Locate every Plasmodium parasite.
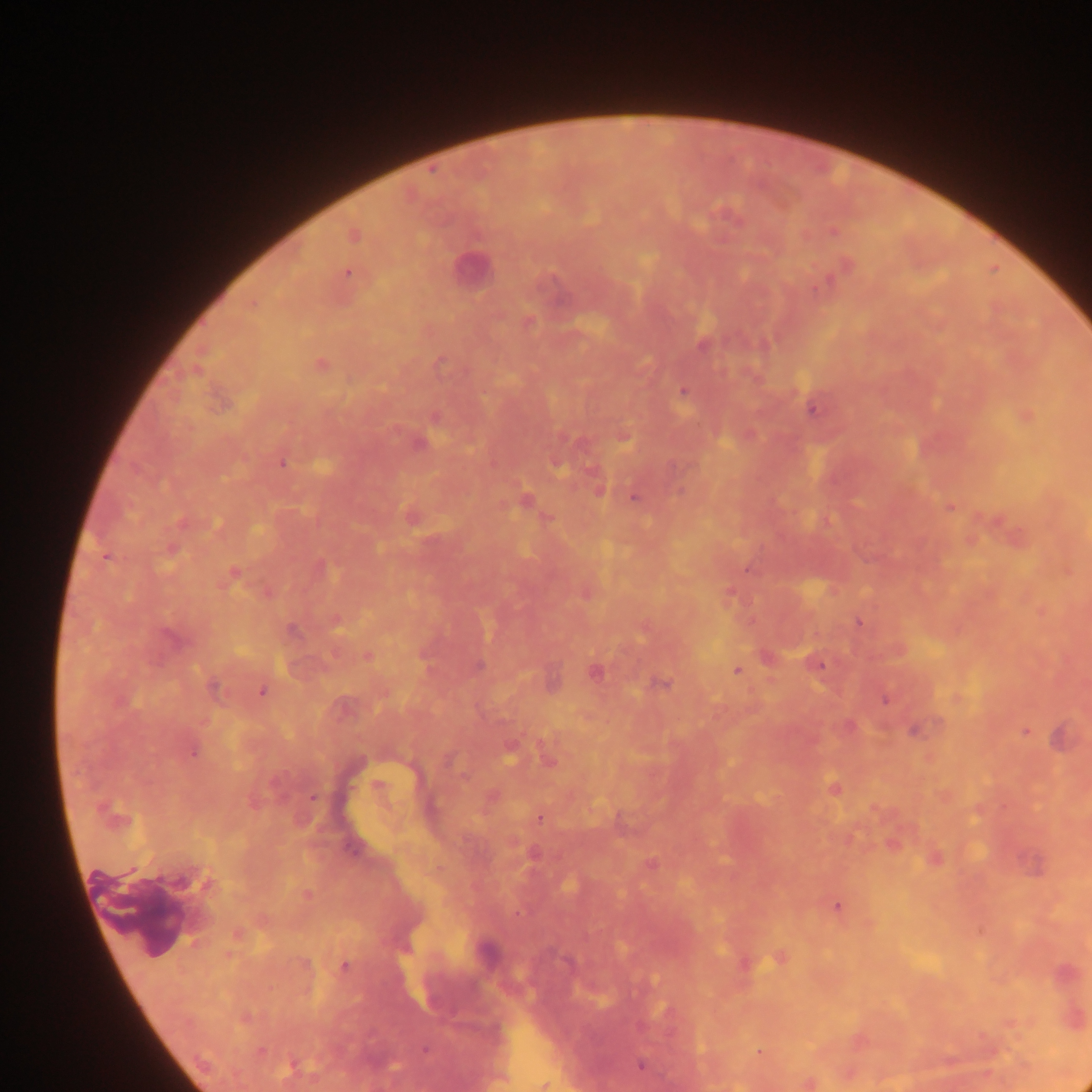

Approximate centers as [x, y] in pixels.
Plasmodium parasites: [727, 217], [834, 233], [353, 235], [847, 264], [347, 273], [527, 322], [702, 346], [320, 365], [684, 391], [812, 410], [436, 417], [623, 437], [419, 443], [282, 464], [556, 465], [599, 491], [679, 493], [634, 498], [524, 501], [950, 506], [106, 557], [233, 573], [859, 622], [291, 630], [171, 638], [367, 656], [816, 664], [479, 665], [737, 670], [595, 672], [662, 684], [215, 689], [261, 692], [884, 698], [915, 730], [1024, 731], [1063, 738], [193, 751], [509, 751], [548, 760], [448, 761], [834, 787], [313, 798], [539, 818], [651, 864], [184, 881], [204, 883], [307, 894], [837, 907], [779, 959], [343, 966], [425, 1050], [261, 1051], [760, 1052], [292, 1065], [640, 1065], [808, 1082].

Summary:
  - Leukocyte locations: [469, 268]
  - Country: Ghana
  - Image size: 1092×1092 pixels
  - Field of view: single
  - Preparation: thick blood smear
  - Capture: mobile-phone photograph through a microscope